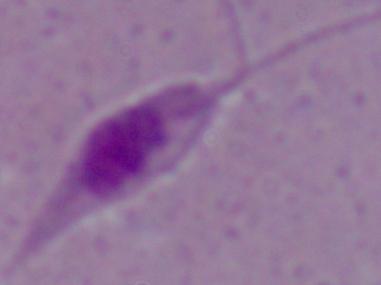

identification: Leishmania
magnification: 1000x
modality: micrograph